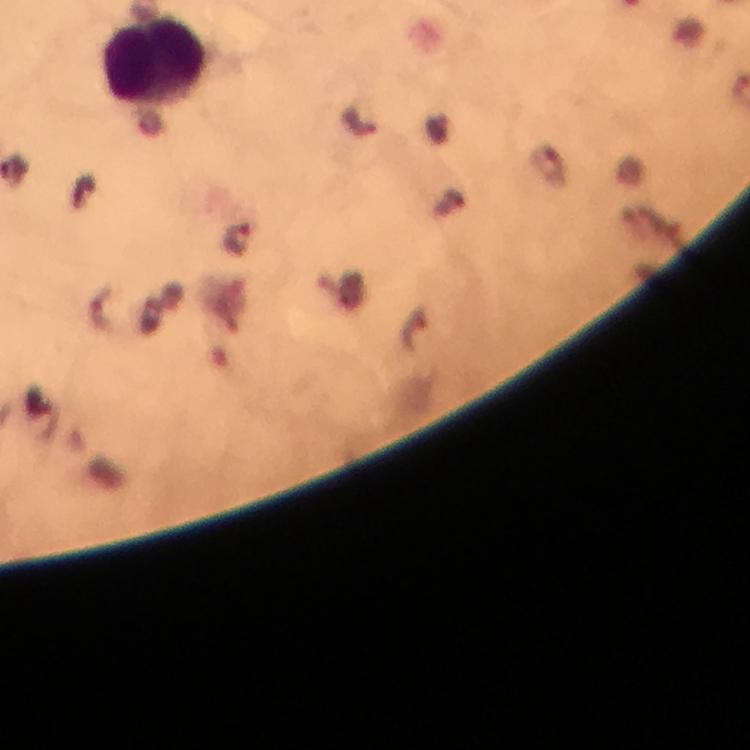
{
  "image_size": "750×750 pixels",
  "cropped_from": "a single field of view",
  "magnification": "100x",
  "plasmodium_parasite_locations": "approximate centers as {x, y} in pixels: {238, 240}",
  "immersion_oil": "applied",
  "context": "from a malaria diagnostic workup",
  "preparation": "thick blood film",
  "stain": "Giemsa",
  "capture": "smartphone mounted on the microscope",
  "leukocyte_locations": "approximate centers as {x, y} in pixels: {155, 62}"
}